Classify this cell by malaria status.
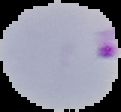

Parasitized.

Image is 121×112 pixels. The area outside the segmented cell region is set to black. From a thin blood smear.